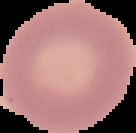 Malaria status: uninfected. From a thin blood smear. Image is 136×133 pixels. Segmented cell region on a black background.